Name the cell type shown.
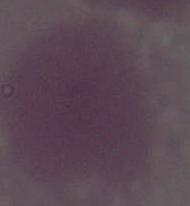
This is an erythrocyte.

modality: photomicrograph
magnification: 1000x